Assess this cell for malaria.
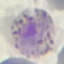

It is parasitized.

Summary:
  - Stain: Giemsa
  - Preparation: thin smear
  - Capture: smartphone through the microscope eyepiece
  - Image type: automatically extracted cell patch, resized to 64 × 64 pixels